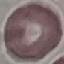

Result: no malaria parasites detected. Photographed with a smartphone camera at the microscope eyepiece. Thin blood smear. Giemsa stain. Cell patch, automatically extracted from a larger field of view and resized to 64 × 64 pixels.